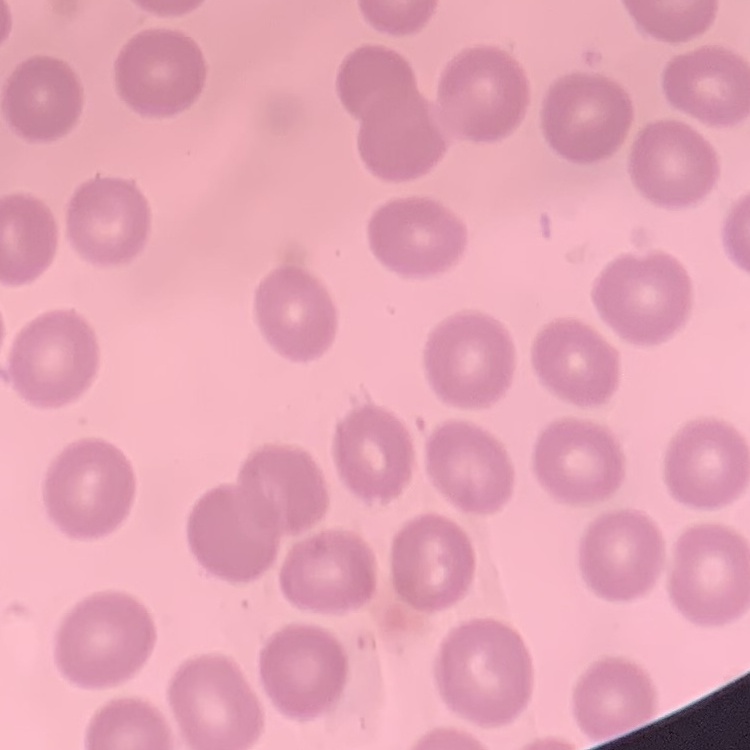
{
  "erythrocyte_morphology": "no rouleaux formation",
  "preparation": "thin peripheral smear",
  "image_type": "one tile cut from a larger photomicrograph",
  "stain": "Field's or Giemsa"
}